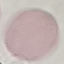

malaria status = uninfected
preparation = thin blood smear
image type = cell patch, automatically extracted from a larger field of view and resized to 64 × 64 pixels
capture = smartphone through the microscope eyepiece
stain = Giemsa